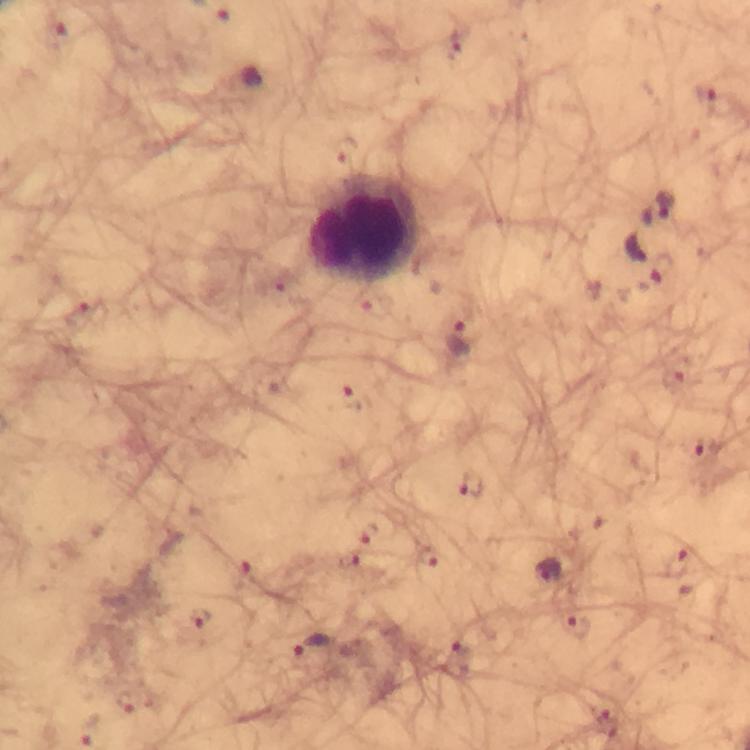

{
  "immersion_oil": "used",
  "cropped_from": "a single field of view",
  "preparation": "thick blood film",
  "capture": "smartphone camera through the microscope",
  "leukocyte_locations": "approximate centers as [x, y] in pixels: [363, 230]",
  "stain": "Giemsa",
  "context": "from a malaria diagnostic workup",
  "image_size": "750×750 pixels",
  "plasmodium_parasite_locations": "approximate centers as [x, y] in pixels: [706, 100], [658, 209], [647, 259], [460, 340], [703, 449], [471, 485], [368, 532], [429, 557], [678, 564], [547, 569], [202, 618], [575, 626], [311, 645], [456, 659]",
  "magnification": "100x"
}